Comment on the morphology of the erythrocytes.
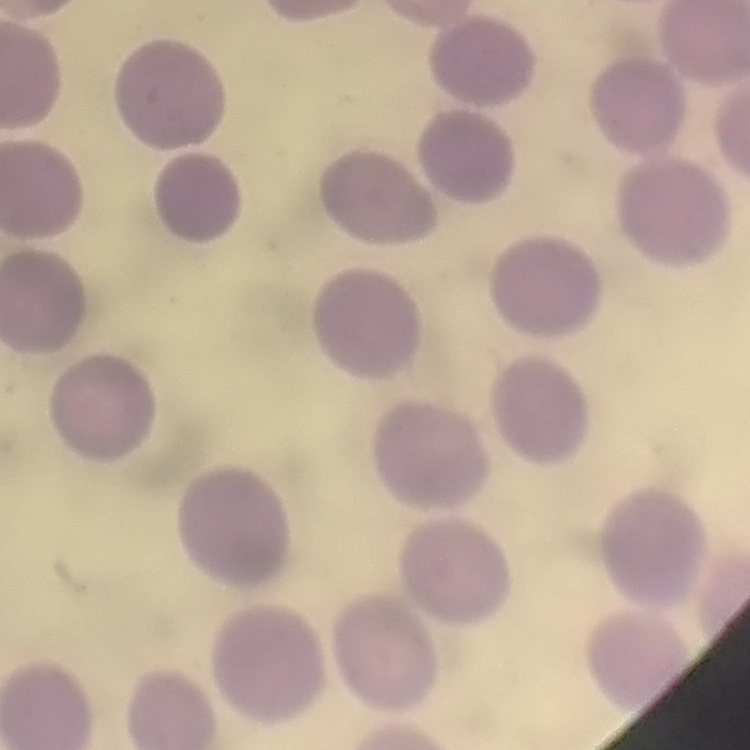
They show no rouleaux formation.

image type = one tile cut from a larger photomicrograph
stain = Field's or Giemsa
preparation = thin blood film